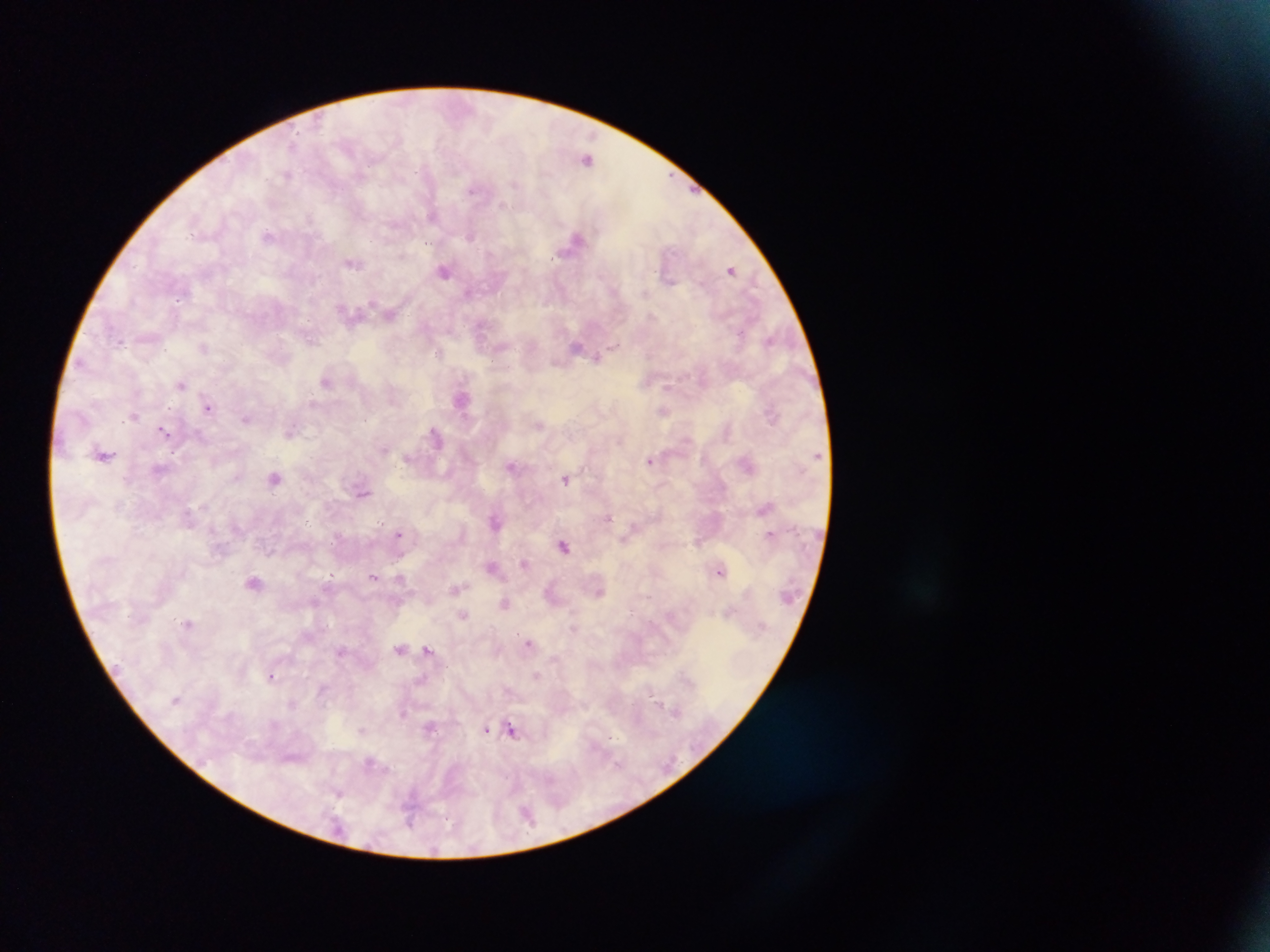
Approximate centers as {x, y} in pixels. Plasmodium parasite locations: {294, 144}, {587, 159}, {287, 175}, {516, 184}, {474, 189}, {503, 205}, {433, 216}, {309, 217}, {268, 235}, {470, 235}, {575, 238}, {352, 264}, {730, 270}, {444, 271}, {468, 293}, {179, 299}, {391, 314}, {313, 340}, {770, 340}, {121, 344}, {577, 346}, {613, 346}, {204, 348}, {438, 353}, {597, 357}, {326, 381}, {182, 384}, {667, 386}, {462, 398}, {208, 408}, {664, 411}, {134, 416}, {246, 418}, {539, 424}, {164, 430}, {291, 430}, {435, 436}, {619, 441}, {384, 448}, {104, 455}, {650, 460}, {511, 465}, {236, 477}, {275, 478}, {566, 479}, {363, 493}, {609, 518}, {496, 521}, {399, 533}, {770, 534}, {564, 545}, {524, 563}, {492, 567}, {721, 571}, {331, 575}, {373, 576}, {400, 578}, {254, 581}, {455, 589}, {600, 592}, {505, 604}, {462, 616}, {187, 622}, {529, 643}, {427, 648}, {400, 649}, {340, 651}, {271, 676}, {537, 676}, {323, 690}, {651, 694}, {656, 700}, {292, 704}, {675, 711}, {403, 712}, {431, 727}, {486, 729}, {362, 731}, {513, 731}, {612, 738}, {369, 762}, {617, 764}, {339, 794}, {410, 812}, {527, 814}, {409, 821}. One field of view. Sample from Ghana. Image is 1270×952 pixels. Thick blood film. Mobile-phone photograph taken through the microscope.